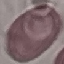
result: no malaria parasites detected
stain: Giemsa
preparation: thin blood smear
capture: smartphone camera at the microscope eyepiece
image_type: cell patch, automatically extracted from a larger field of view and resized to 64 × 64 pixels